Identify the parasite.
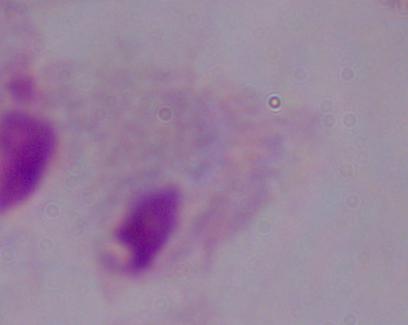
This is a trichomonad.

Summary:
  - Modality: photomicrograph
  - Magnification: 1000x